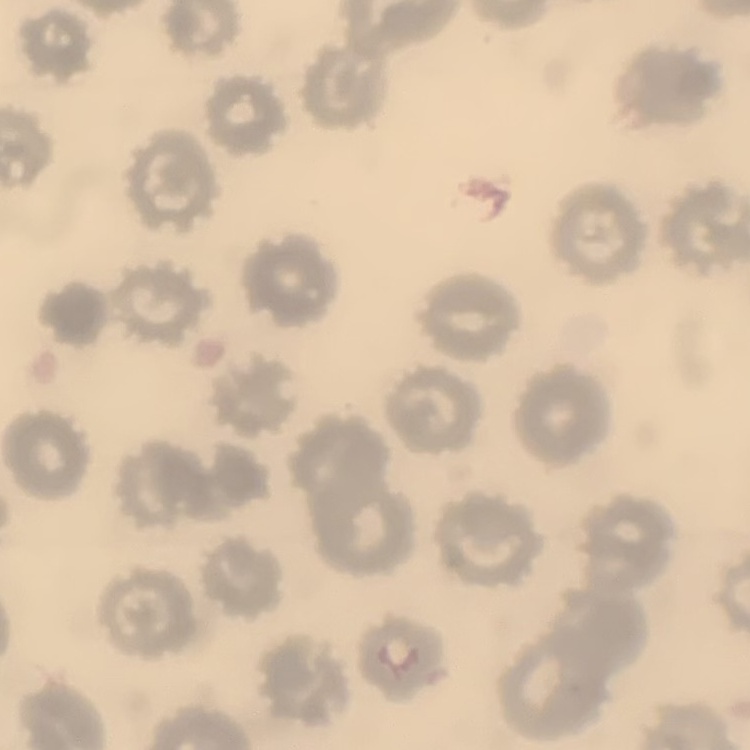
erythrocyte morphology = no rouleaux formation
stain = Field's or Giemsa
image type = one tile cut from a larger photomicrograph
preparation = thin blood film